Assess this cell for malaria.
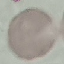

It is uninfected.

Thin blood smear. Automatically extracted cell patch, resized to 64 × 64 pixels. Acquired by smartphone through the microscope eyepiece. Giemsa-stained preparation.